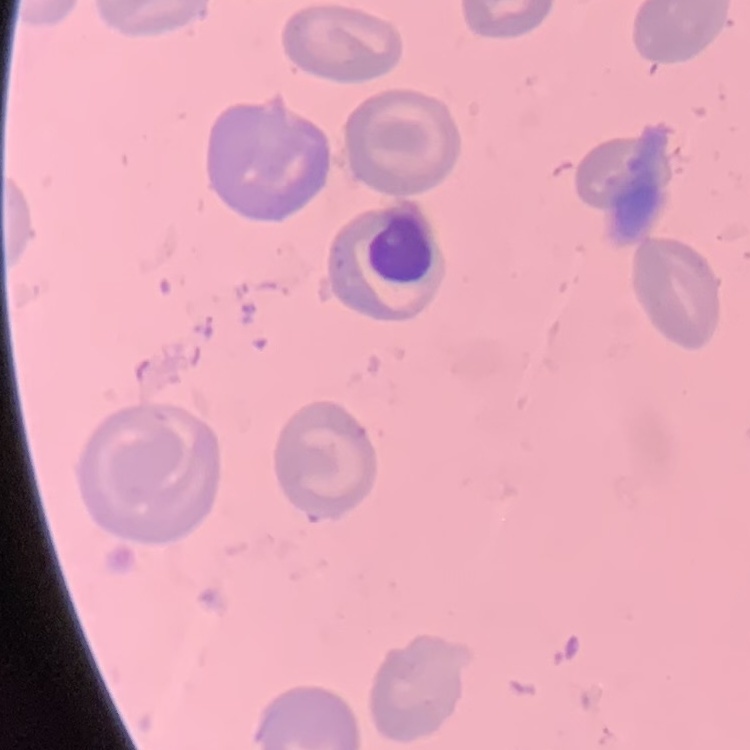
The erythrocytes show no rouleaux formation. Stained with either Field's or Giemsa. Thin peripheral smear. Square crop of a larger photomicrograph.